Identify the preparation type.
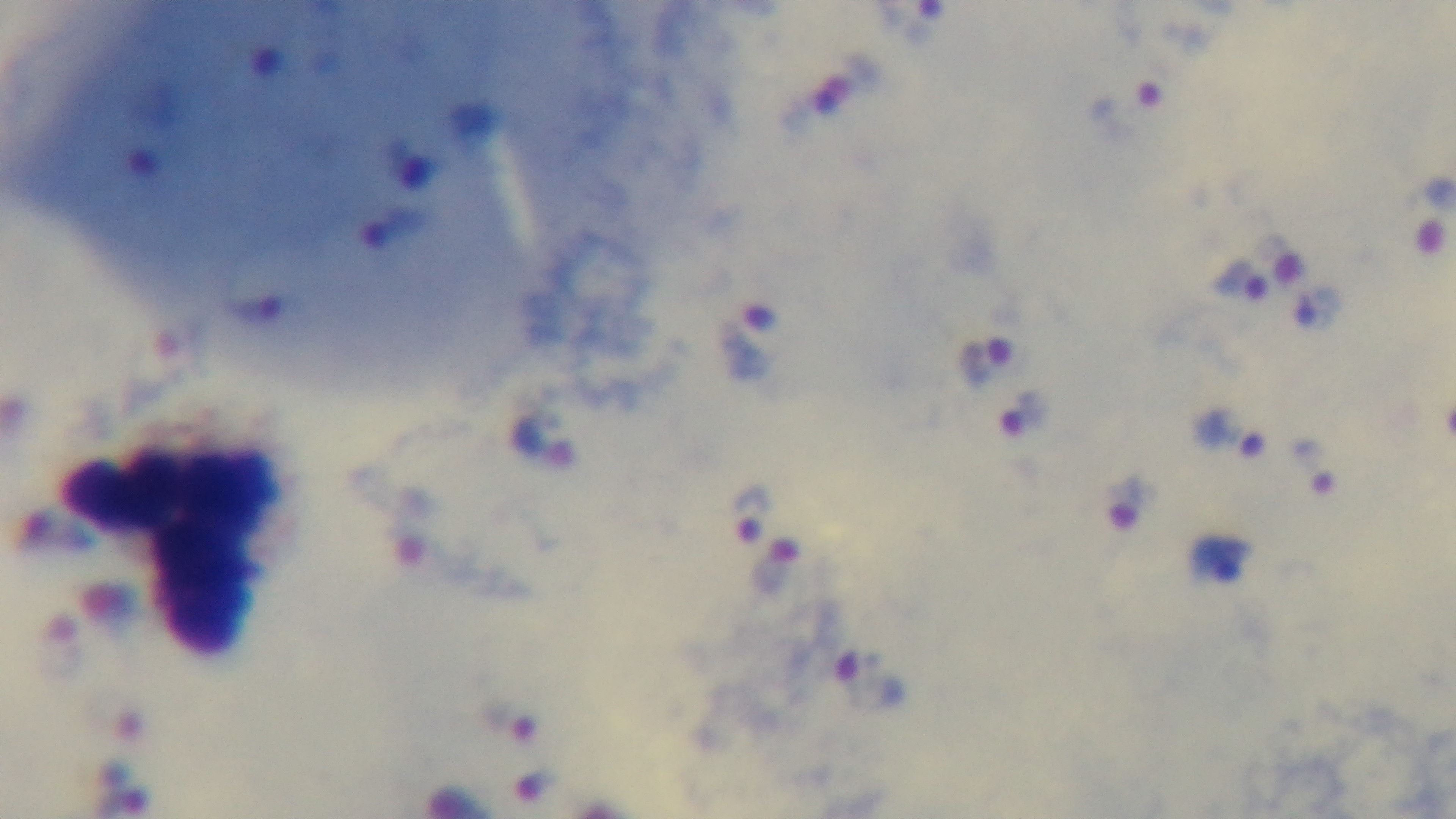
A thick smear.

Summary:
  - Stain: Giemsa
  - Malaria status: positive
  - Modality: light microscopy
  - Capture: mounted 4K digital camera
  - Objective: 100x oil immersion
  - Field of view: one from the slide